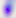

Summary:
  - Identification: Toxoplasma gondii
  - Modality: micrograph
  - Magnification: 400x